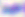

Captured at 400x magnification. Micrograph. Toxoplasma gondii is shown.